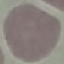
malaria status = uninfected
preparation = thin blood film
capture = smartphone camera at the microscope eyepiece
image type = cell patch, automatically extracted from a larger field of view and resized to 64 × 64 pixels
stain = Giemsa